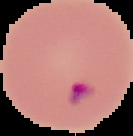

Summary:
  - Image type: cell region segmented out of the field of view; surrounding area masked to black
  - Preparation: thin blood smear
  - Malaria status: parasitized
  - Image size: 133×136 pixels